State the blood parasite species.
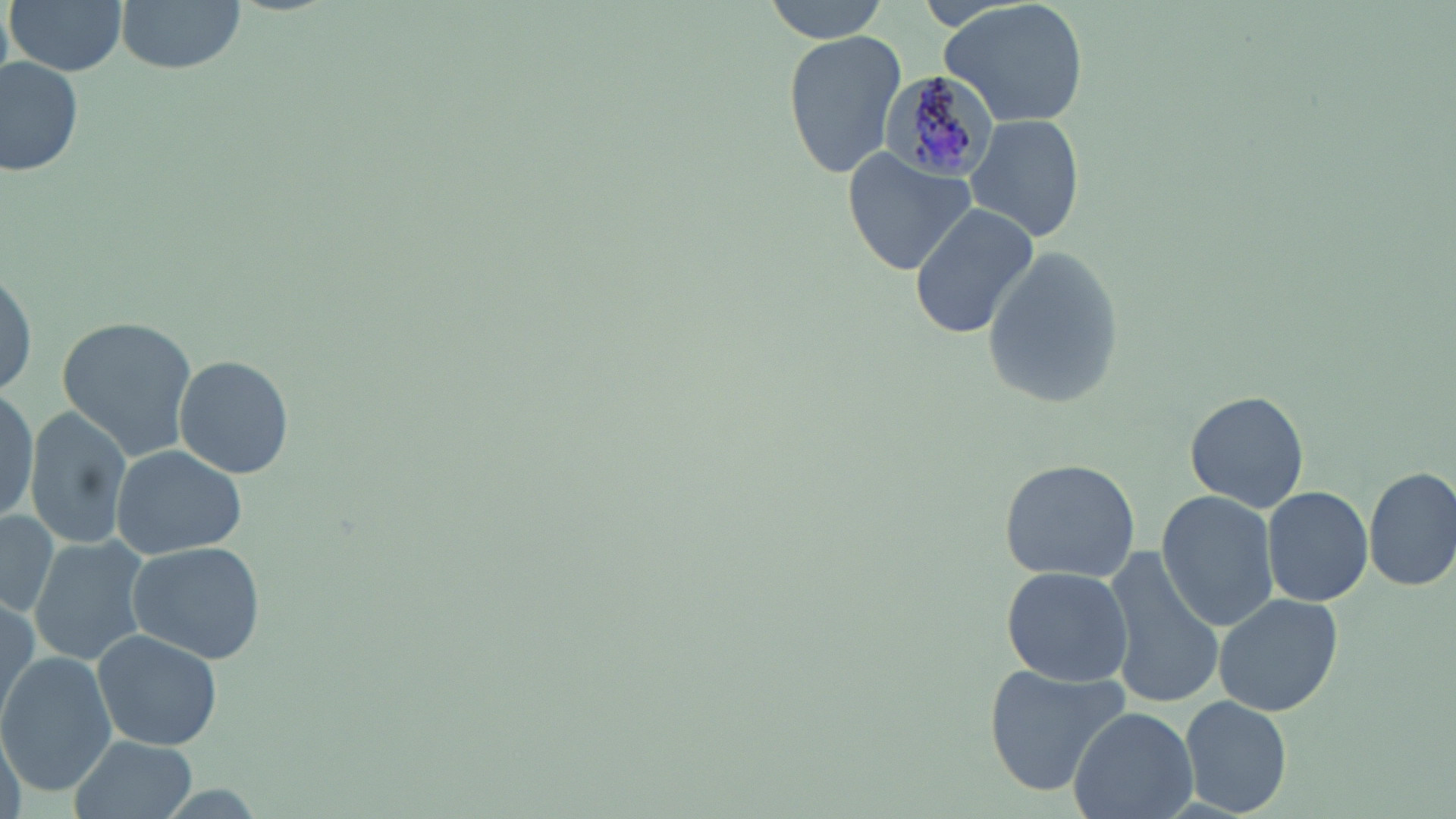
Plasmodium malariae.

magnification = 1000x
image size = 1456×819 pixels
field of view = single
uninfected red blood cell locations = approximate bounding boxes as [x1, y1, x2, y2] in pixels: [8, 0, 128, 76], [117, 0, 245, 74], [763, 0, 891, 40], [939, 0, 1088, 129], [782, 29, 908, 182], [1, 57, 83, 178], [965, 113, 1086, 245], [843, 149, 977, 274], [908, 202, 1041, 341], [982, 245, 1123, 408], [0, 261, 38, 407], [55, 314, 199, 461], [173, 356, 295, 479], [0, 384, 37, 529], [1185, 392, 1309, 512], [25, 406, 135, 548], [111, 443, 245, 558], [998, 457, 1140, 582], [1363, 467, 1456, 592], [1263, 485, 1374, 607], [1155, 490, 1278, 633], [0, 506, 62, 618], [126, 537, 265, 664], [30, 538, 147, 666], [1101, 545, 1226, 709], [1000, 566, 1132, 685], [0, 588, 40, 728], [1212, 591, 1347, 718], [92, 628, 222, 751], [0, 652, 115, 797], [984, 664, 1131, 796], [1179, 693, 1292, 817], [1069, 707, 1197, 819], [0, 724, 26, 819], [71, 734, 198, 819]
modality = optical microscopy
Plasmodium malariae-infected red blood cell locations = approximate bounding boxes as [x1, y1, x2, y2] in pixels: [875, 72, 998, 185]
stain = May-Grünwald-Giemsa
preparation = thin blood smear